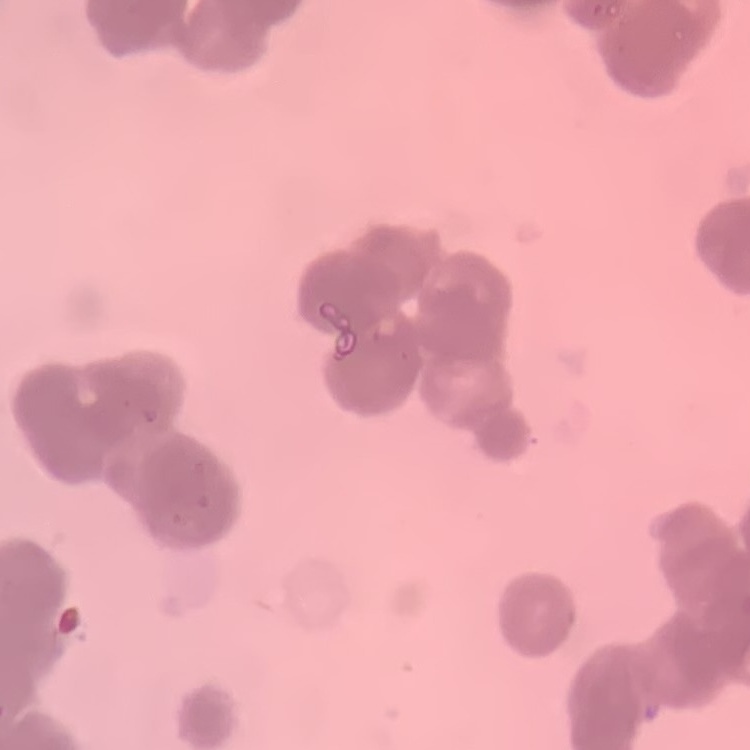

Summary:
  - Erythrocyte morphology: rouleaux formation
  - Preparation: thin peripheral smear
  - Stain: Field's or Giemsa
  - Image type: one tile cut from a larger photomicrograph